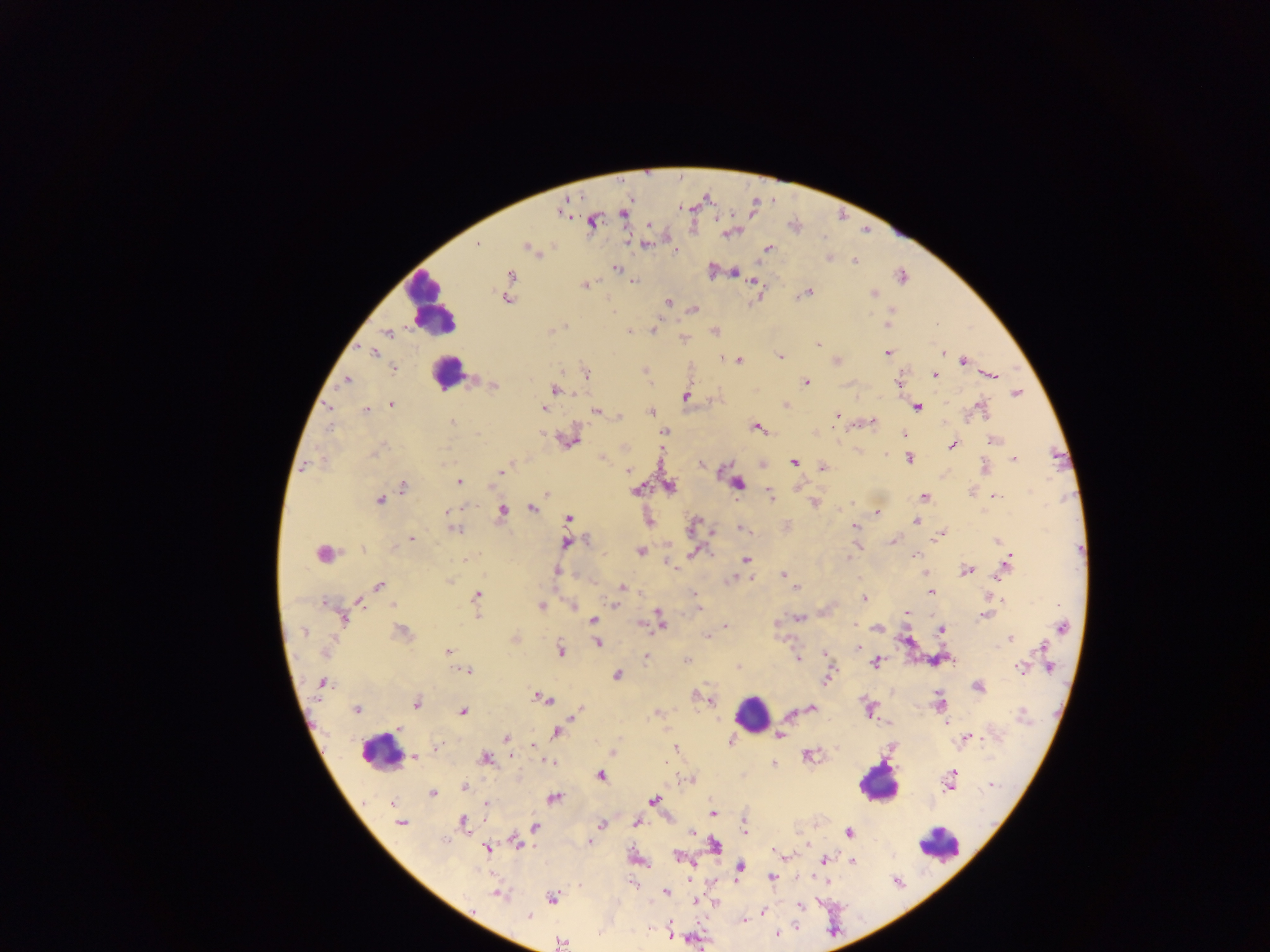

{
  "leukocyte_locations": "approximate centers as {x, y} in pixels: {433, 306}, {447, 373}, {752, 713}, {380, 751}, {878, 783}, {939, 844}",
  "plasmodium_parasite_locations": "approximate centers as {x, y} in pixels: {564, 207}, {624, 212}, {592, 221}, {729, 232}, {645, 243}, {476, 244}, {528, 247}, {767, 248}, {676, 250}, {829, 259}, {854, 261}, {616, 267}, {711, 269}, {733, 272}, {510, 276}, {901, 276}, {633, 280}, {754, 281}, {584, 285}, {807, 292}, {873, 293}, {506, 298}, {668, 303}, {693, 308}, {890, 313}, {887, 323}, {936, 323}, {654, 329}, {551, 330}, {714, 330}, {629, 331}, {387, 333}, {684, 338}, {816, 343}, {375, 352}, {887, 352}, {940, 353}, {779, 357}, {738, 360}, {835, 361}, {963, 361}, {393, 368}, {645, 371}, {586, 372}, {933, 374}, {989, 375}, {347, 380}, {806, 382}, {493, 384}, {899, 384}, {555, 389}, {1016, 392}, {686, 395}, {548, 397}, {392, 404}, {785, 405}, {916, 407}, {541, 408}, {981, 408}, {365, 409}, {597, 411}, {651, 411}, {836, 415}, {617, 416}, {872, 421}, {451, 422}, {757, 427}, {664, 431}, {904, 434}, {567, 438}, {993, 440}, {951, 445}, {660, 450}, {886, 456}, {602, 457}, {907, 458}, {1014, 458}, {793, 462}, {761, 463}, {307, 464}, {702, 464}, {823, 466}, {985, 468}, {501, 470}, {627, 470}, {458, 481}, {737, 483}, {669, 486}, {403, 487}, {797, 487}, {637, 490}, {971, 491}, {769, 493}, {545, 494}, {924, 497}, {997, 497}, {380, 500}, {813, 502}, {531, 508}, {503, 510}, {448, 511}, {876, 513}, {649, 518}, {568, 519}, {915, 521}, {693, 525}, {788, 526}, {855, 527}, {454, 528}, {742, 528}, {710, 533}, {939, 534}, {410, 538}, {892, 540}, {997, 540}, {566, 543}, {856, 545}, {362, 548}, {639, 551}, {694, 553}, {324, 554}, {745, 559}, {668, 562}, {1005, 565}, {966, 570}, {556, 571}, {924, 573}, {782, 574}, {750, 577}, {996, 577}, {730, 579}, {449, 580}, {378, 586}, {622, 587}, {795, 588}, {931, 592}, {695, 595}, {476, 596}, {863, 597}, {359, 600}, {1002, 600}, {393, 604}, {614, 604}, {541, 605}, {574, 605}, {698, 608}, {906, 613}, {477, 615}, {984, 615}, {343, 616}, {798, 617}, {659, 618}, {592, 620}, {640, 623}, {775, 624}, {854, 624}, {726, 626}, {877, 627}, {1061, 628}, {940, 629}, {305, 631}, {401, 632}, {707, 636}, {1011, 638}, {514, 639}, {907, 641}, {597, 642}, {1043, 646}, {858, 647}, {559, 651}, {448, 652}, {324, 653}, {825, 655}, {647, 656}, {797, 658}, {686, 661}, {874, 663}, {738, 667}, {1020, 667}, {1049, 668}, {468, 671}, {616, 675}, {826, 678}, {321, 683}, {978, 687}, {693, 695}, {538, 696}, {544, 698}, {710, 700}, {416, 702}, {939, 702}, {810, 708}, {356, 709}, {869, 709}, {462, 712}, {578, 712}, {657, 713}, {946, 723}, {400, 727}, {950, 730}, {556, 732}, {779, 735}, {966, 737}, {506, 738}, {533, 744}, {676, 748}, {614, 751}, {807, 755}, {413, 756}, {510, 756}, {484, 758}, {549, 761}, {773, 764}, {599, 775}, {691, 779}, {950, 782}, {991, 784}, {463, 787}, {432, 792}, {553, 798}, {653, 800}, {391, 804}, {485, 805}, {712, 812}, {636, 821}, {400, 823}, {463, 823}, {600, 824}, {535, 827}, {744, 830}, {693, 831}, {848, 832}, {517, 841}, {591, 842}, {714, 845}, {487, 849}, {778, 854}, {785, 856}, {677, 857}, {823, 859}, {853, 861}, {739, 867}, {772, 877}, {827, 883}, {665, 891}, {497, 894}, {551, 897}, {693, 900}, {715, 902}, {800, 906}, {762, 911}, {527, 916}, {742, 919}, {669, 930}, {776, 932}, {561, 943}",
  "preparation": "thick blood smear",
  "capture": "mobile-phone photograph through a microscope",
  "field_of_view": "single",
  "country": "Ghana",
  "image_size": "1270×952 pixels"
}